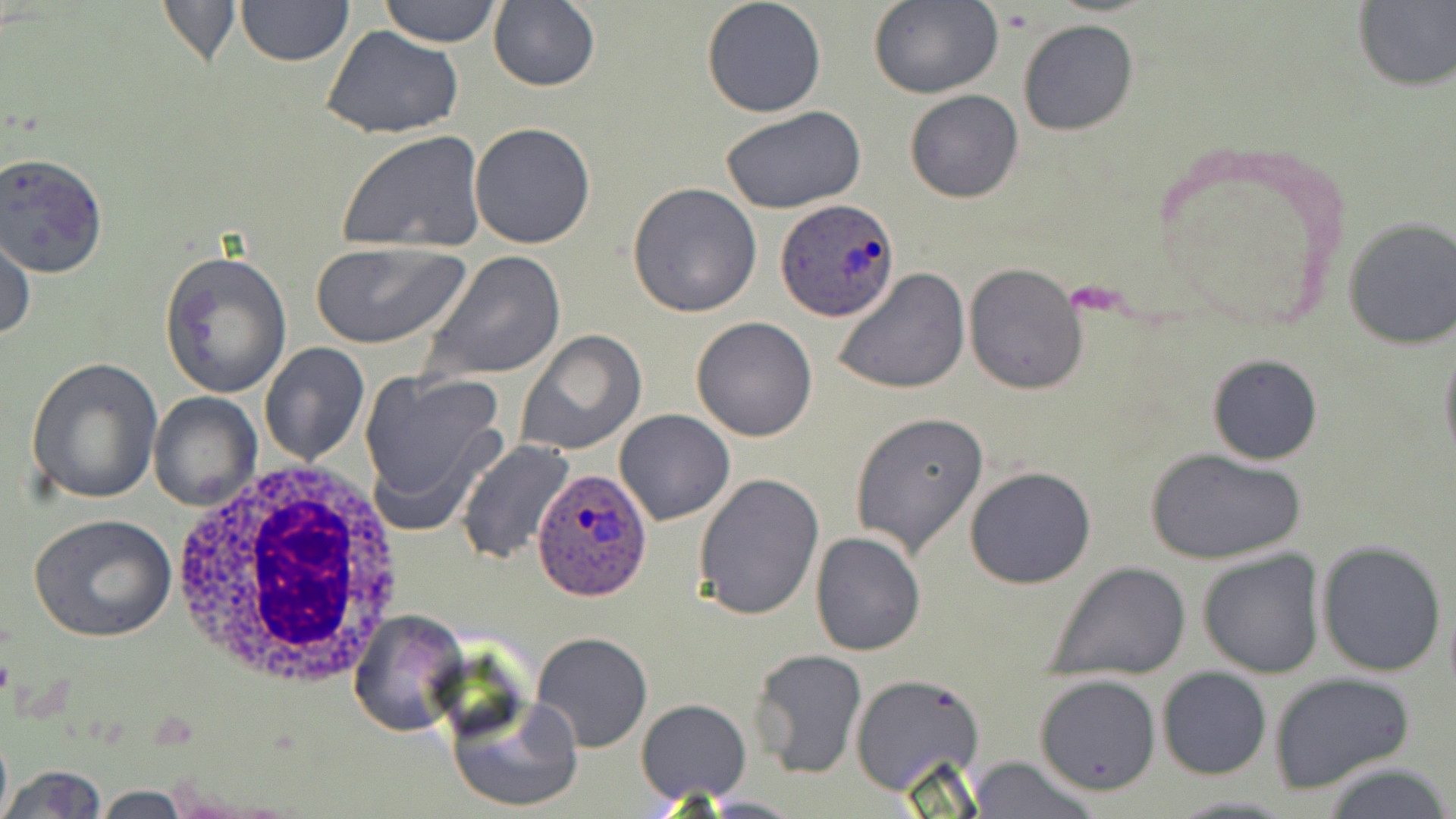
{
  "slide_level_diagnosis": "Plasmodium ovale",
  "stain": "May-Grünwald-Giemsa",
  "uninfected_red_blood_cell_locations": "approximate bounding boxes as [x1, y1, x2, y2] in pixels: [155, 0, 243, 68], [235, 0, 352, 66], [377, 0, 503, 47], [700, 0, 827, 119], [867, 1, 1003, 100], [1352, 2, 1456, 90], [488, 3, 601, 91], [1016, 19, 1139, 137], [321, 24, 465, 141], [904, 90, 1024, 204], [720, 104, 866, 214], [469, 122, 597, 250], [337, 129, 487, 253], [0, 153, 108, 279], [627, 182, 762, 318], [1344, 218, 1456, 349], [0, 232, 35, 344], [311, 240, 469, 350], [160, 249, 292, 397], [420, 250, 566, 384], [963, 263, 1089, 394], [831, 270, 970, 395], [691, 316, 820, 442], [516, 331, 648, 456], [1438, 332, 1456, 471], [261, 343, 369, 467], [1206, 354, 1323, 466], [26, 357, 162, 504], [358, 370, 507, 528], [148, 393, 261, 510], [614, 408, 735, 526], [849, 413, 990, 558], [458, 439, 578, 565], [1147, 448, 1305, 566], [964, 465, 1096, 589], [693, 472, 824, 619], [29, 514, 178, 644], [810, 531, 926, 657], [1316, 539, 1448, 678], [1197, 549, 1325, 680], [1046, 563, 1191, 680], [347, 610, 469, 738], [530, 631, 653, 752], [751, 648, 867, 780], [1156, 666, 1272, 780], [849, 672, 987, 798], [1269, 672, 1416, 794], [1033, 673, 1162, 795], [446, 694, 583, 815], [635, 698, 752, 804], [966, 754, 1100, 819], [1318, 760, 1455, 819], [3, 764, 108, 819], [1165, 793, 1298, 818], [701, 795, 806, 816]",
  "field_of_view": "single",
  "image_size": "1456×819 pixels",
  "white_blood_cell_locations": "approximate bounding boxes as [x1, y1, x2, y2] in pixels: [167, 460, 412, 689]",
  "plasmodium_ovale_infected_red_blood_cell_locations": "approximate bounding boxes as [x1, y1, x2, y2] in pixels: [775, 196, 900, 322], [531, 468, 655, 600]",
  "preparation": "thin blood film",
  "modality": "optical microscopy",
  "magnification": "1000x"
}